Give the position of every Plasmodium parasite visible.
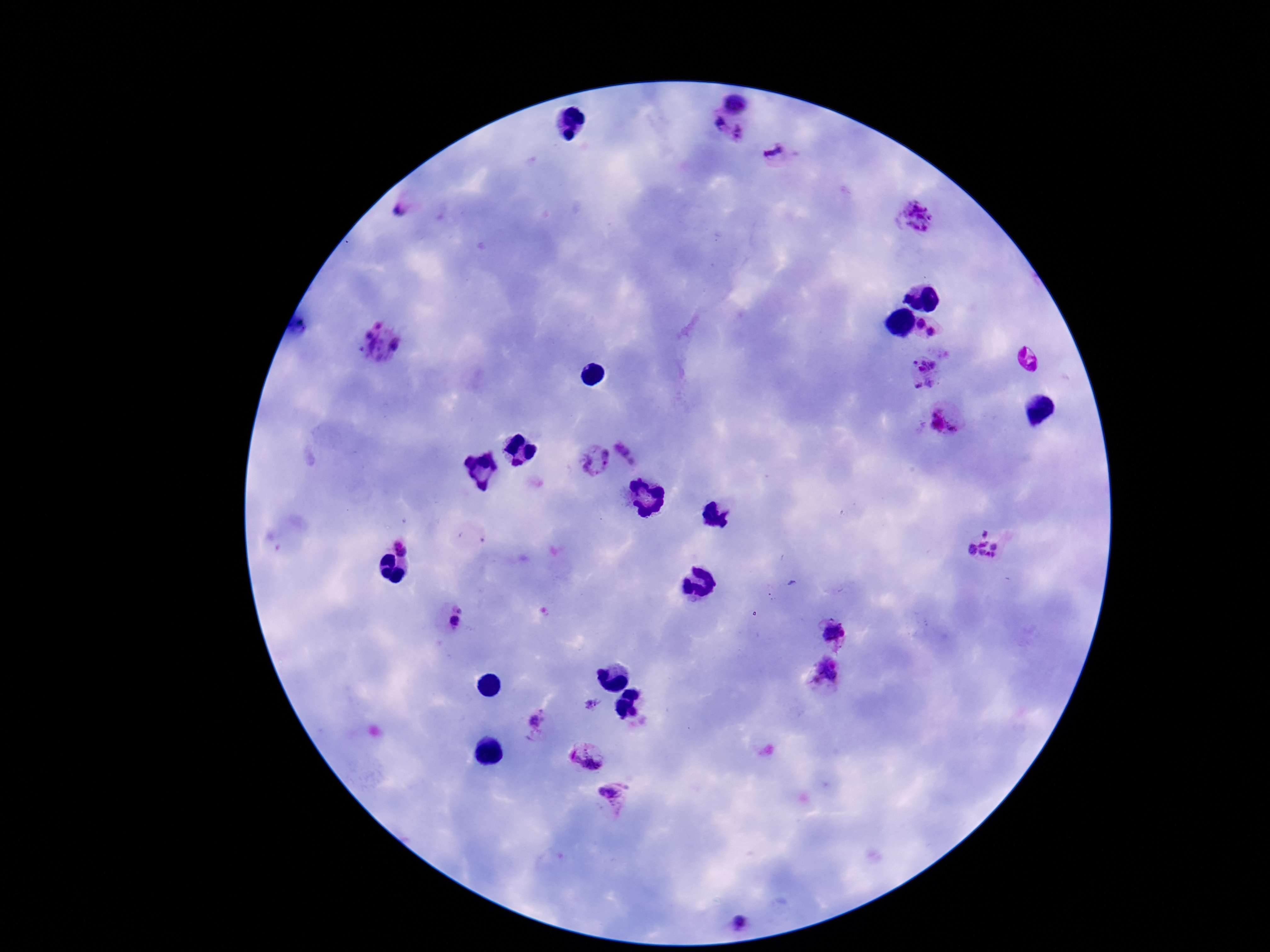

Approximate centers as (x, y) in pixels.
Plasmodium parasites: (738, 100), (719, 126), (741, 136), (776, 152), (404, 208), (921, 220), (922, 324), (932, 331), (380, 346), (1029, 360), (925, 373), (946, 419), (629, 454), (594, 460), (979, 545), (403, 547), (454, 616), (833, 633), (827, 671), (540, 722), (587, 756), (612, 795), (737, 922).

magnification = 100x
patient malaria status = positive
field of view = one from this slide
capture = smartphone camera through the microscope eyepiece
preparation = thick blood film
image size = 1270×952 pixels
stain = Giemsa